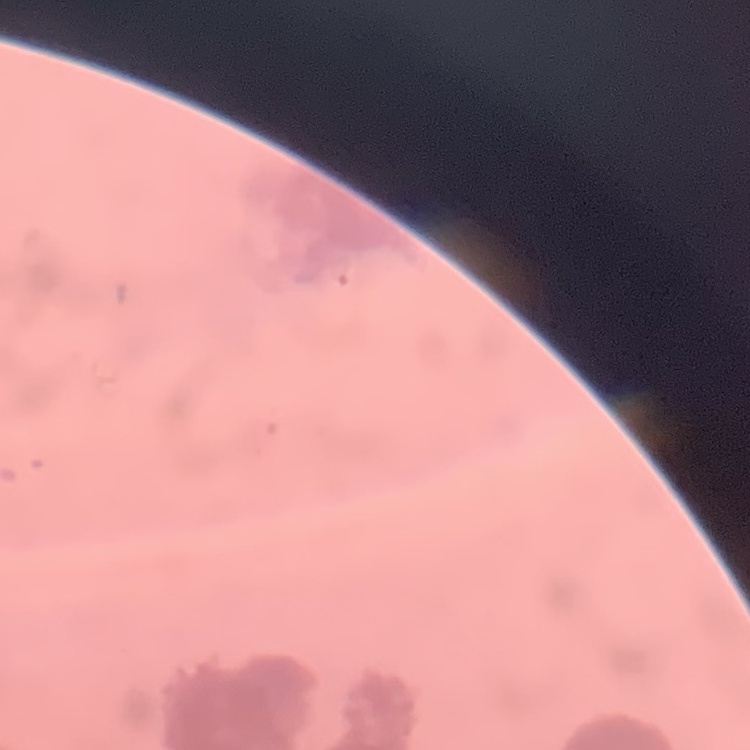
erythrocyte_morphology: rouleaux formation
preparation: thin peripheral smear
stain: Field's or Giemsa
image_type: square crop of a larger photomicrograph